Give the position of every Plasmodium parasite.
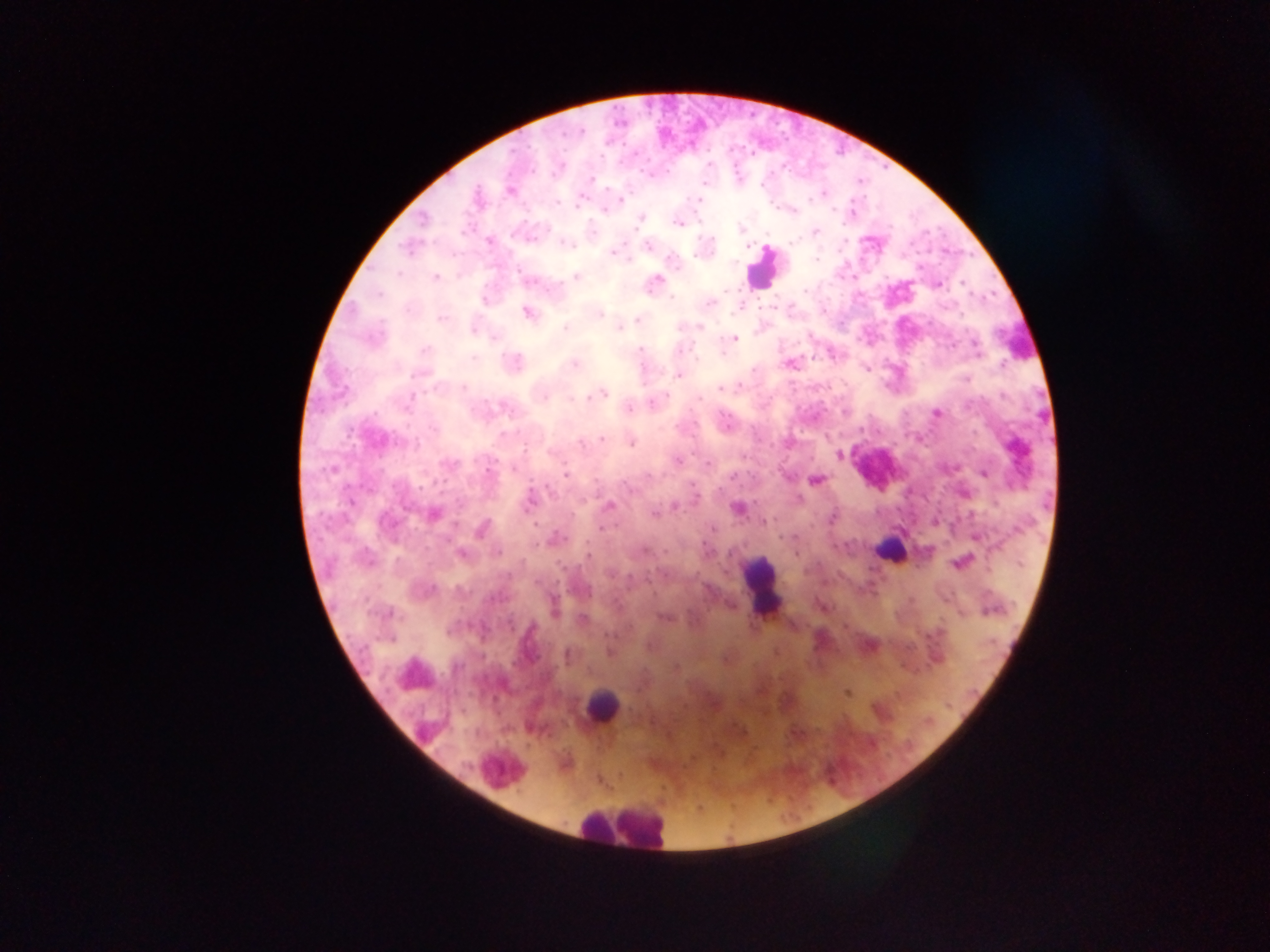
Approximate centers as {x, y} in pixels.
Plasmodium parasites: {589, 178}, {509, 190}, {821, 194}, {699, 200}, {621, 201}, {604, 209}, {792, 210}, {639, 218}, {678, 222}, {814, 232}, {489, 242}, {648, 246}, {614, 251}, {575, 276}, {435, 278}, {529, 280}, {654, 281}, {937, 284}, {710, 303}, {527, 312}, {597, 312}, {442, 318}, {639, 319}, {699, 327}, {566, 328}, {620, 328}, {733, 338}, {425, 349}, {513, 362}, {574, 363}, {790, 364}, {867, 368}, {678, 375}, {598, 394}, {628, 407}, {936, 413}, {602, 438}, {631, 441}, {838, 454}, {677, 460}, {708, 462}, {984, 473}, {815, 480}, {530, 501}, {608, 505}, {737, 509}, {431, 514}, {764, 521}, {482, 528}, {554, 539}, {460, 553}, {796, 553}, {960, 562}, {553, 608}, {663, 618}, {870, 645}, {845, 692}, {797, 734}.

Summary:
  - Leukocyte locations: {763, 268}, {891, 550}, {762, 590}, {601, 707}, {501, 771}, {623, 824}
  - Field of view: single
  - Image size: 1270×952 pixels
  - Country: Ghana
  - Preparation: thick blood smear
  - Capture: mobile-phone photograph through a microscope